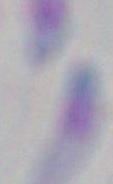
Captured at 1000x magnification. Photomicrograph. Toxoplasma gondii is shown.